Outline each blood parasite and name the species.
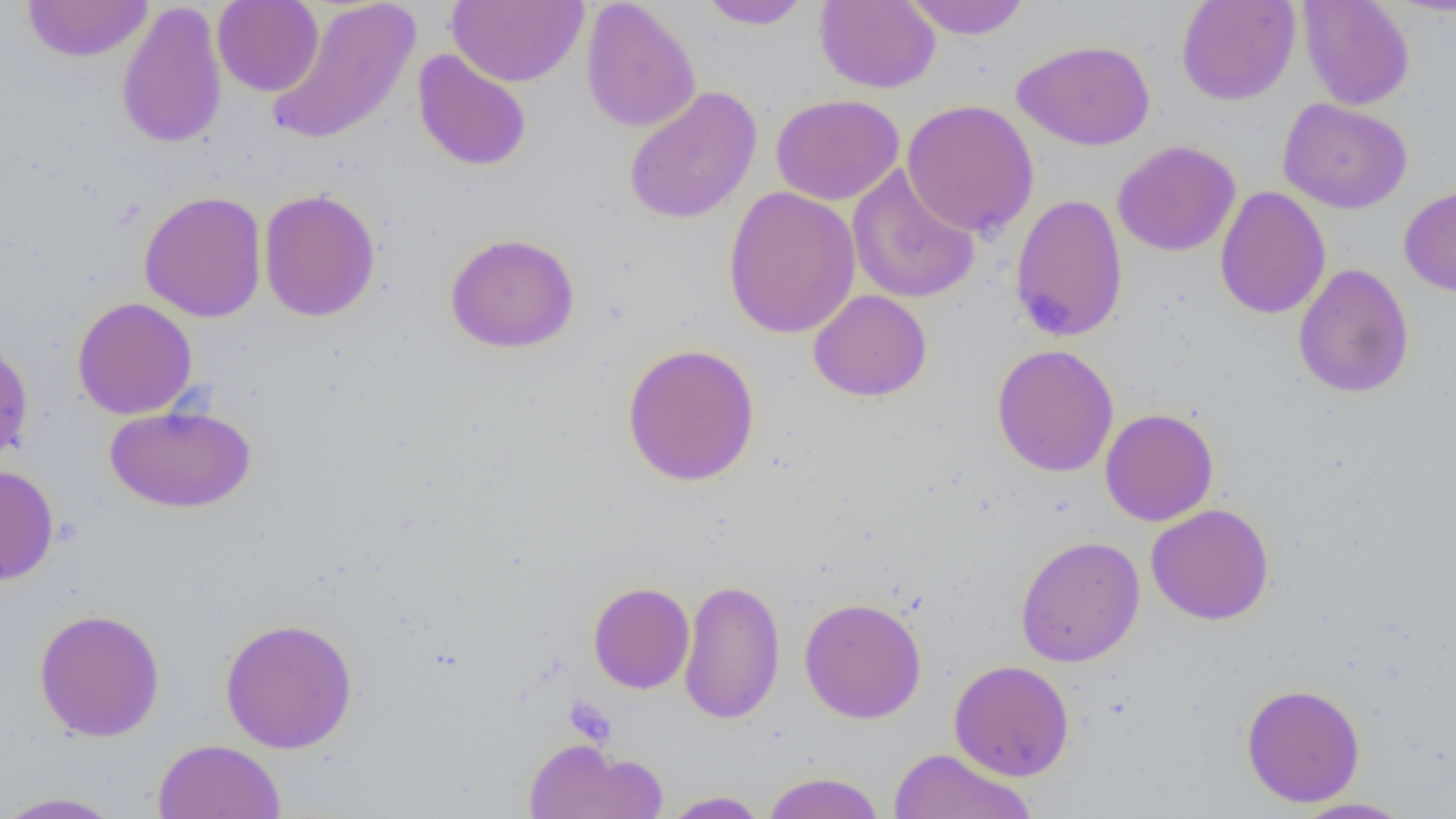
No blood parasites observed.

Approximate bounding boxes as (x1,y1)-(x2,y2) corner pairs in pixels. Uninfected red blood cell locations: (22,0)-(154,63), (265,0)-(421,147), (448,0)-(588,87), (697,0)-(812,30), (901,0)-(1033,39), (1176,0)-(1300,106), (1298,0)-(1415,110), (212,1)-(324,97), (580,1)-(701,133), (814,1)-(941,93), (116,2)-(228,149), (1013,39)-(1155,151), (413,50)-(532,172), (623,85)-(762,225), (770,94)-(904,206), (1278,98)-(1413,214), (901,99)-(1039,238), (1112,140)-(1241,257), (846,164)-(980,305), (1399,183)-(1456,297), (723,186)-(861,340), (1215,186)-(1331,320), (258,189)-(381,322), (138,190)-(267,323), (1009,193)-(1129,343), (445,232)-(580,353), (1293,263)-(1415,398), (808,289)-(932,402), (72,296)-(198,419), (0,337)-(34,468), (621,342)-(760,487), (991,343)-(1119,477), (104,403)-(256,513), (1100,408)-(1219,526), (0,464)-(59,586), (1145,503)-(1275,625), (1014,535)-(1145,667), (679,577)-(785,724), (588,581)-(695,694), (799,596)-(927,724), (33,607)-(166,743), (220,617)-(358,753), (949,659)-(1075,781), (1240,683)-(1365,807), (522,736)-(667,819), (152,738)-(287,818), (888,747)-(1036,818), (761,771)-(885,819), (0,790)-(126,818), (660,790)-(771,818), (1290,797)-(1416,819). Slide-level diagnosis: negative for blood parasites. Single field of view. Optical microscopy. Image is 1456×819 pixels. Thin blood smear. Captured at 1000x magnification.